State which parasite is depicted.
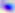
This is Toxoplasma gondii.

Micrograph. 400x magnification.